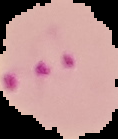
image_type: segmented cell region on a black background
preparation: thin blood film
result: Plasmodium parasites identified
image_size: 118×139 pixels